Comment on the morphology of the red blood cells.
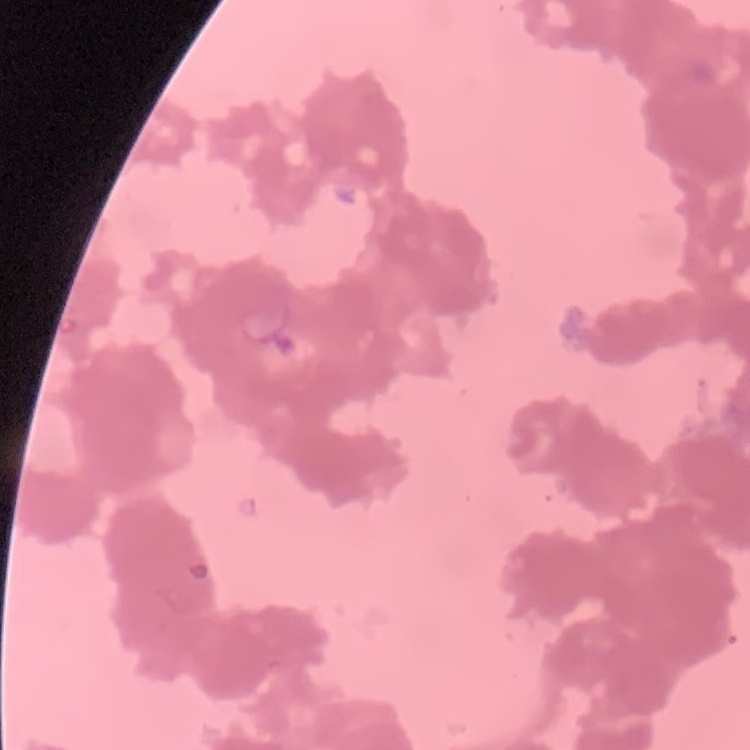
They show rouleaux formation.

Summary:
  - Image type: square crop of a larger photomicrograph
  - Preparation: thin blood film
  - Stain: Field's or Giemsa